Evaluate for parasitized red blood cells.
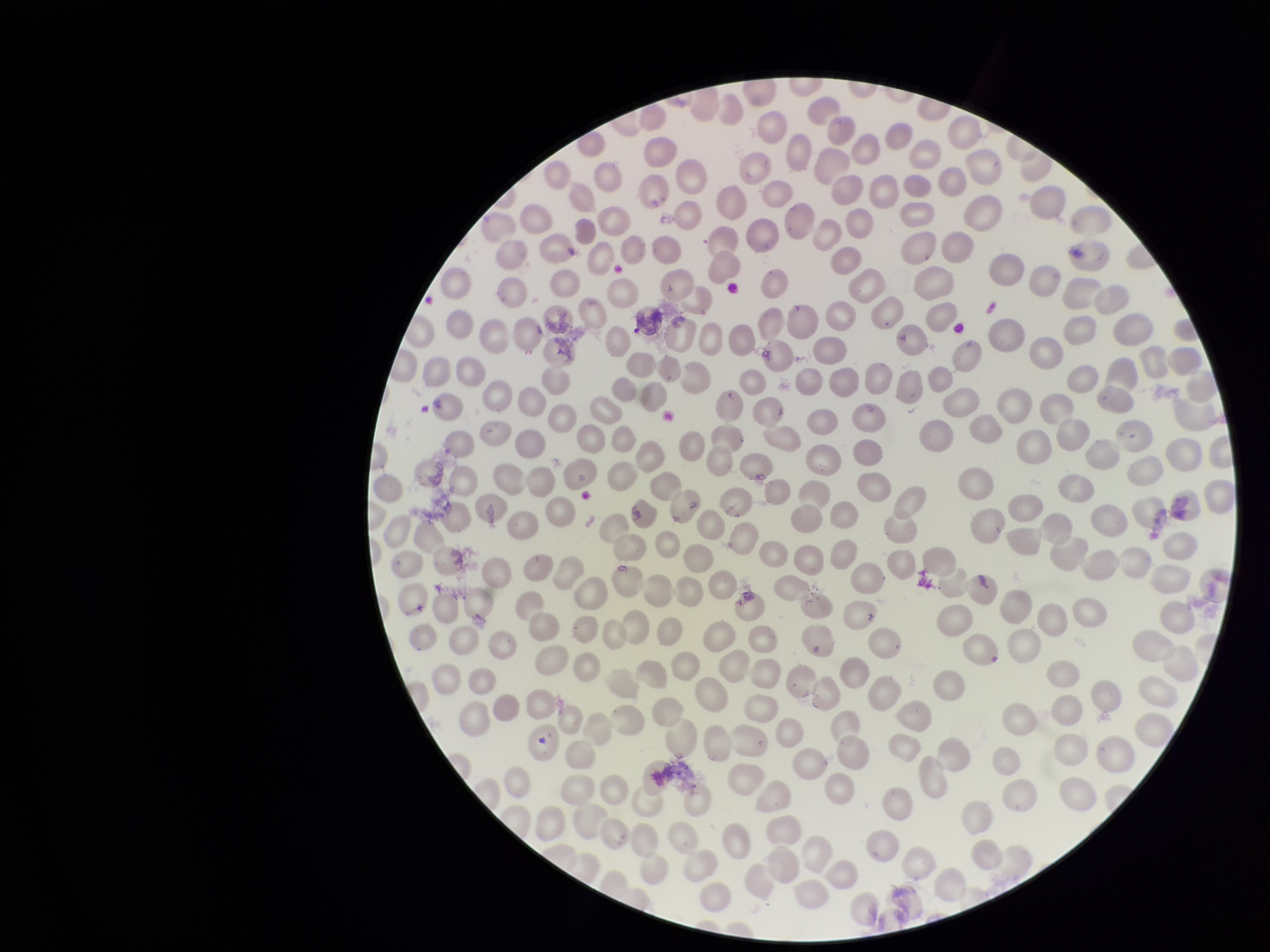
None seen.

{
  "parasitized_red_blood_cell_count": 0,
  "field_of_view": "single",
  "capture": "smartphone photograph through the microscope eyepiece",
  "image_size": "1270×952 pixels",
  "patient_malaria_status": "negative",
  "red_blood_cell_count": 269,
  "preparation": "thin blood smear",
  "stain": "Giemsa"
}